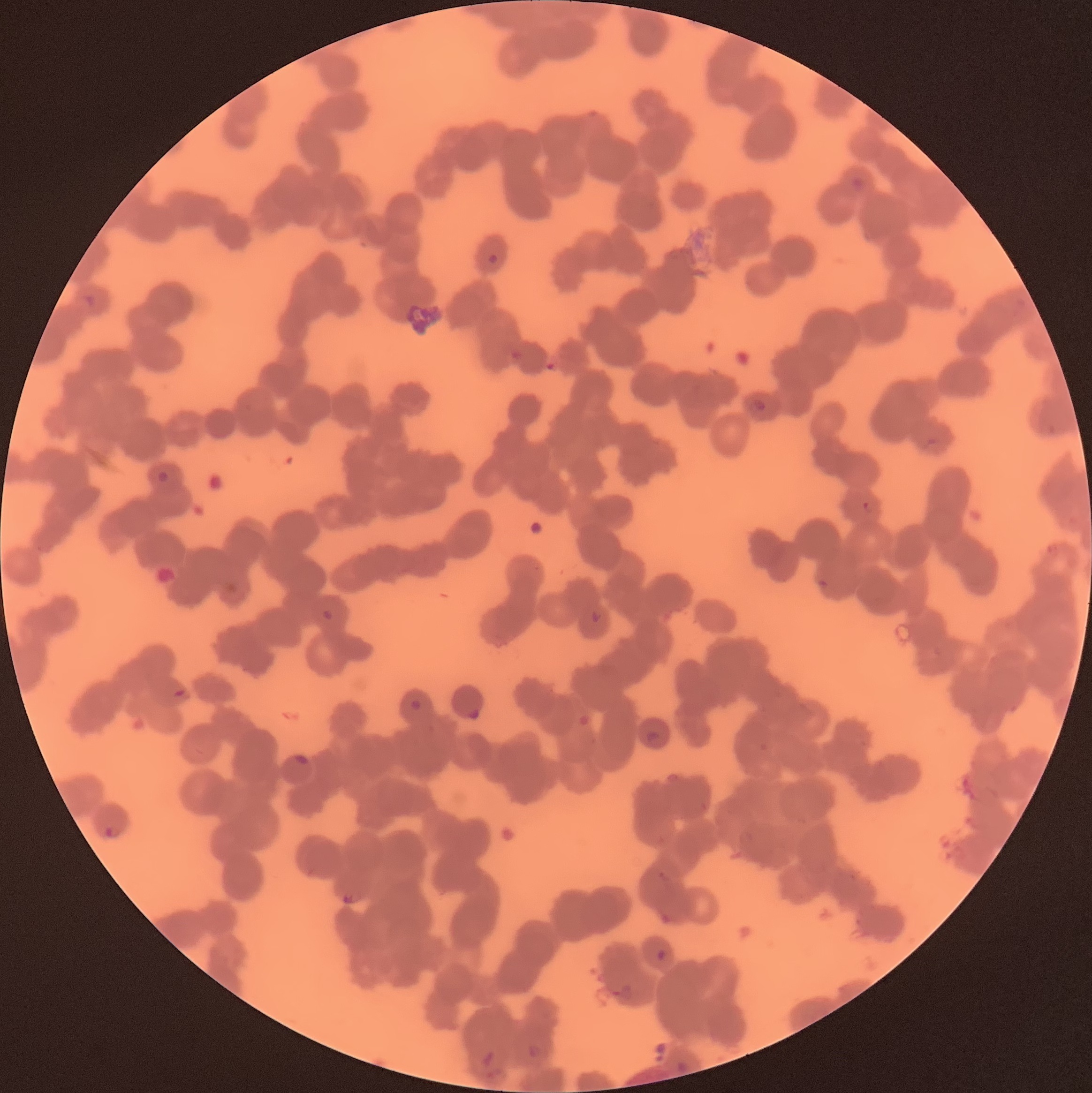
Approximate bounding boxes as (x1, y1, x2, y2) in pixels. Plasmodium parasite locations: (850, 176, 865, 192), (487, 253, 498, 264), (84, 294, 96, 308), (753, 397, 767, 411), (156, 470, 170, 485), (862, 500, 873, 514), (322, 608, 335, 622), (591, 610, 603, 624), (173, 687, 189, 700), (409, 699, 422, 711), (467, 708, 480, 720), (646, 729, 661, 746), (102, 825, 121, 839), (342, 893, 355, 905), (656, 949, 668, 962), (613, 984, 634, 1003), (527, 1044, 544, 1059), (481, 1050, 504, 1078), (676, 1059, 689, 1074). Optical microscopy. Thin blood film. The red blood cells show rouleaux formation. Image is 1092×1093 pixels.